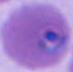

400x or 1000x magnification. A Plasmodium parasite is shown. Micrograph.